Classify this cell by malaria status.
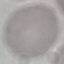
Uninfected.

Summary:
  - Stain: Giemsa
  - Capture: smartphone camera at the microscope eyepiece
  - Image type: cell patch, automatically extracted from a larger field of view and resized to 64 × 64 pixels
  - Preparation: thin smear